Comment on the morphology of the red blood cells.
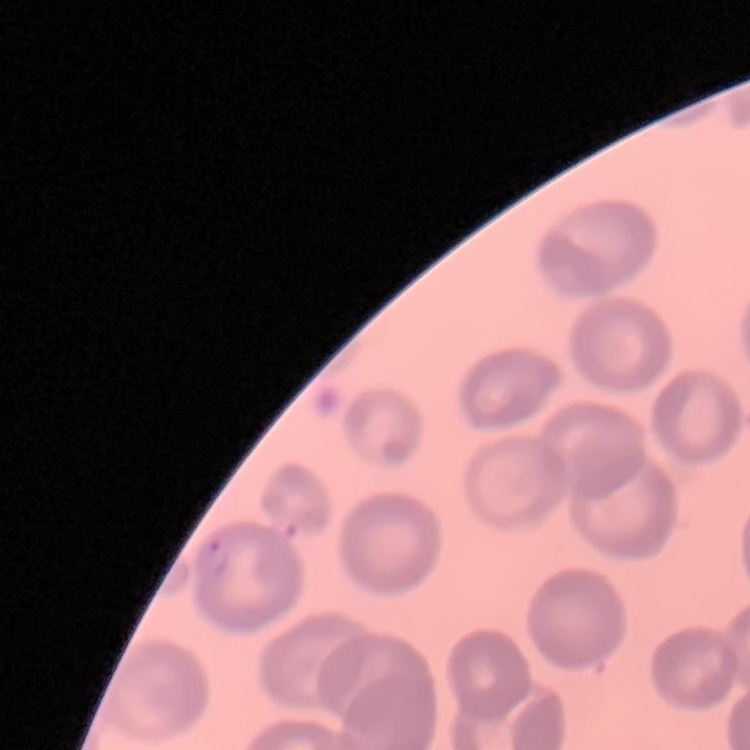

They show no rouleaux formation.

Summary:
  - Stain: Field's or Giemsa
  - Image type: square crop of a larger photomicrograph
  - Preparation: thin peripheral smear